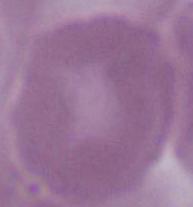
Summary:
  - Modality: photomicrograph
  - Magnification: 1000x
  - Identification: red blood cell